State which parasite is depicted.
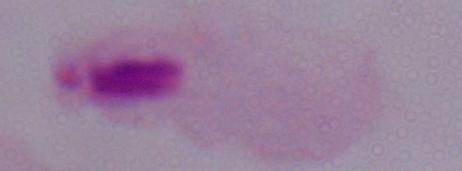
A trichomonad.

Summary:
  - Magnification: 1000x
  - Modality: photomicrograph